Classify this cell by malaria status.
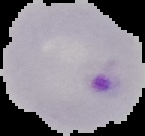

Parasitized.

preparation = thin blood smear
image type = segmented cell region on a black background
image size = 145×136 pixels